Identify the parasite.
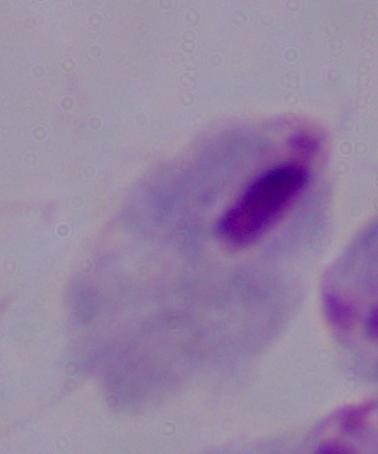

A trichomonad.

modality = photomicrograph
magnification = 1000x